Give the position of every leukocyte.
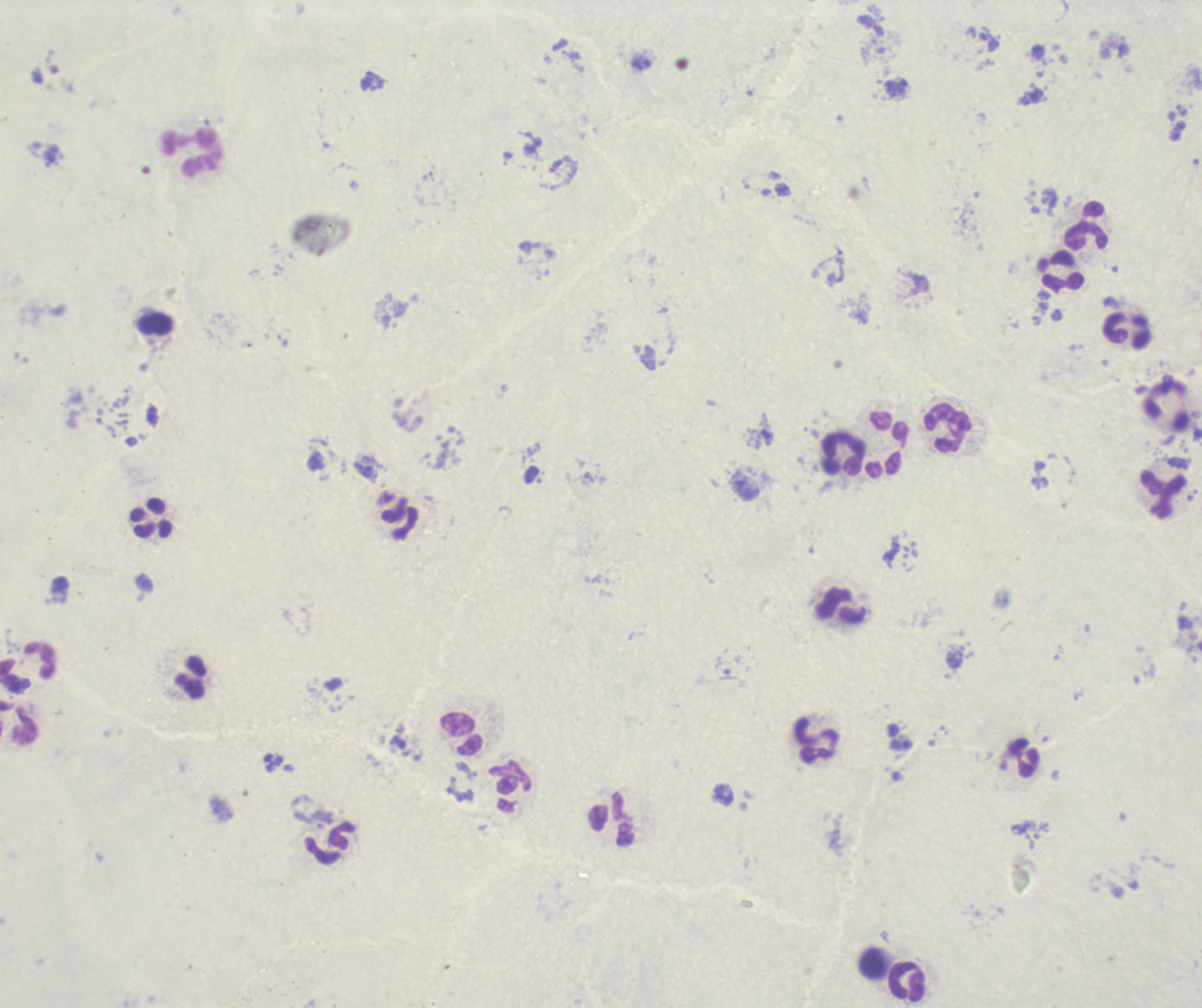

Approximate object centers, in pixels from the top-left corner.
Leukocytes: (x=192, y=153), (x=1086, y=227), (x=1061, y=271), (x=1126, y=331), (x=1166, y=405), (x=948, y=428), (x=886, y=444), (x=844, y=453), (x=1162, y=494), (x=151, y=520), (x=401, y=520), (x=842, y=606), (x=20, y=722), (x=461, y=733), (x=815, y=740), (x=1023, y=758), (x=511, y=788), (x=612, y=820), (x=328, y=843), (x=873, y=962), (x=907, y=981).

Result: no Plasmodium parasites detected. Image is 1202×1008 pixels. Single field of view. Captured at 100x magnification. Previously used in an actual diagnosis. Background quality: unsatisfactory. Romanowsky stain. Thick blood smear.